Classify this cell by malaria status.
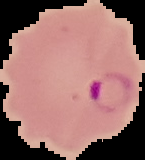

It is parasitized.

Image is 145×160 pixels. From a thin blood film. The area outside the segmented cell region is set to black.